Describe the morphology of the red blood cells.
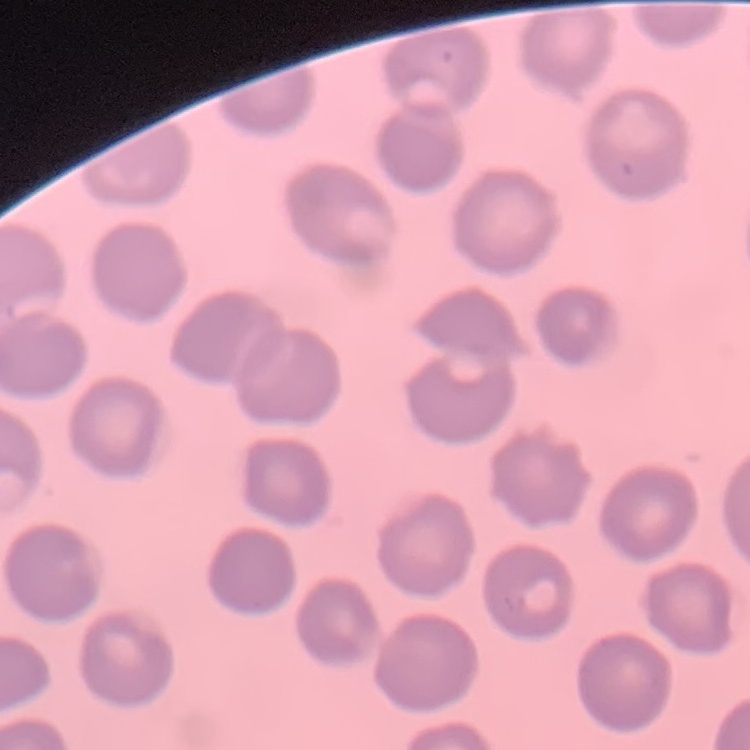
They show no rouleaux formation.

{
  "image_type": "square crop of a larger photomicrograph",
  "preparation": "thin blood film",
  "stain": "Field's or Giemsa"
}